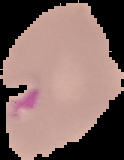
image size = 124×160 pixels
image type = segmented cell region with the area outside set to black
malaria status = parasitized
preparation = thin blood film